Name the blood parasite species.
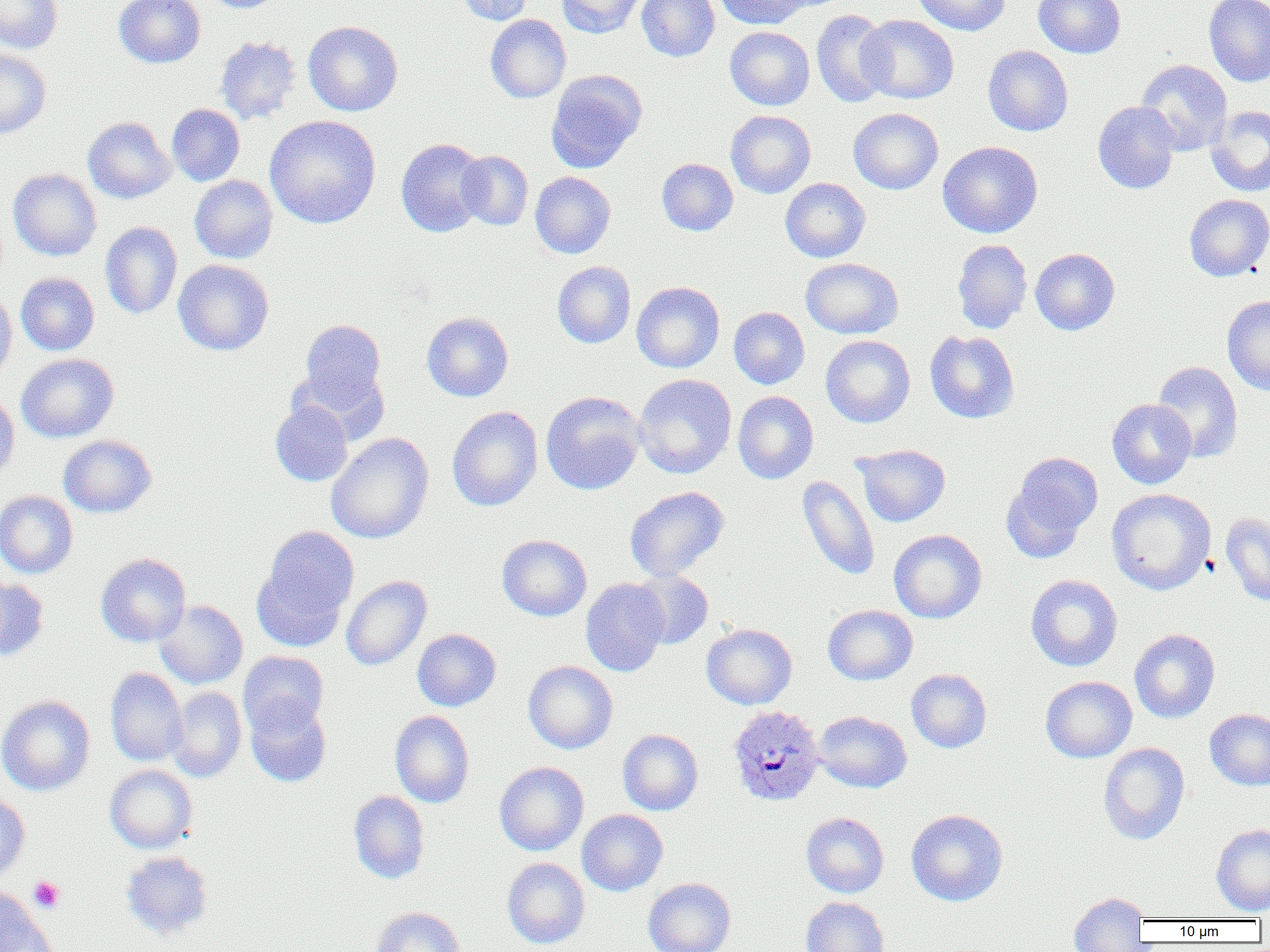
Plasmodium ovale.

{
  "platelet_locations": "approximate bounding boxes as [x1, y1, x2, y2] in pixels: [29, 876, 64, 912]",
  "preparation": "thin blood smear",
  "uninfected_red_blood_cell_locations": "approximate bounding boxes as [x1, y1, x2, y2] in pixels: [0, 0, 62, 53], [114, 0, 205, 68], [206, 0, 285, 13], [452, 0, 535, 25], [556, 0, 646, 38], [636, 0, 720, 62], [714, 0, 811, 29], [912, 0, 1010, 35], [1034, 0, 1126, 59], [1204, 0, 1270, 87], [811, 9, 892, 108], [485, 14, 571, 103], [856, 15, 959, 104], [303, 21, 403, 116], [725, 26, 815, 110], [215, 36, 301, 125], [983, 45, 1073, 136], [0, 48, 51, 139], [1135, 59, 1233, 155], [546, 70, 647, 173], [1092, 101, 1181, 194], [166, 104, 244, 186], [1206, 105, 1270, 197], [848, 107, 943, 194], [726, 110, 816, 198], [264, 114, 381, 228], [82, 116, 175, 204], [396, 138, 488, 238], [937, 141, 1042, 238], [456, 151, 533, 230], [657, 158, 738, 235], [8, 169, 102, 261], [530, 172, 615, 258], [189, 175, 277, 263], [780, 178, 870, 263], [1184, 194, 1270, 281], [100, 222, 182, 319], [952, 239, 1032, 333], [1030, 248, 1120, 335], [801, 258, 903, 339], [173, 259, 274, 356], [552, 261, 636, 348], [15, 272, 99, 356], [632, 282, 724, 372], [0, 289, 17, 388], [1222, 295, 1270, 395], [729, 307, 809, 389], [422, 312, 513, 402], [299, 319, 386, 408], [925, 330, 1019, 423], [821, 335, 915, 428], [16, 353, 118, 442], [1152, 361, 1243, 462], [634, 374, 736, 479], [0, 391, 19, 481], [541, 391, 645, 495], [733, 391, 818, 484], [1107, 399, 1196, 489], [270, 401, 352, 486], [447, 406, 543, 512], [326, 433, 433, 543], [58, 435, 156, 518], [853, 444, 950, 527], [1002, 452, 1102, 559], [797, 475, 880, 580], [625, 486, 729, 581], [1106, 488, 1216, 594], [0, 490, 78, 578], [1220, 512, 1270, 606], [254, 526, 359, 647], [888, 529, 987, 623], [496, 534, 592, 621], [96, 553, 191, 646], [630, 570, 713, 649], [1025, 574, 1123, 672], [340, 575, 432, 670], [0, 577, 48, 661], [581, 578, 669, 676], [154, 599, 248, 689], [823, 605, 917, 685], [701, 623, 797, 710], [412, 629, 501, 711], [1129, 629, 1220, 723], [238, 651, 329, 735], [523, 661, 618, 754], [105, 668, 188, 766], [906, 668, 992, 753], [1040, 676, 1137, 763], [167, 687, 246, 782], [0, 695, 95, 796], [244, 695, 331, 787], [1205, 709, 1270, 791], [390, 711, 474, 807], [813, 711, 912, 793], [618, 729, 703, 815], [1098, 742, 1190, 845], [494, 762, 589, 855], [105, 765, 197, 853], [348, 790, 430, 883], [0, 794, 30, 884], [577, 809, 668, 896], [906, 809, 1008, 906], [801, 812, 889, 898], [1210, 824, 1270, 915], [120, 850, 213, 939], [502, 858, 590, 948], [643, 877, 736, 952], [0, 886, 39, 951], [1068, 892, 1149, 951], [801, 897, 889, 952], [371, 906, 466, 952], [2, 909, 59, 952]",
  "image_size": "1270×952 pixels",
  "plasmodium_ovale_infected_red_blood_cell_locations": "approximate bounding boxes as [x1, y1, x2, y2] in pixels: [728, 704, 825, 807]",
  "modality": "optical microscopy",
  "magnification": "1000x",
  "field_of_view": "one of a larger specimen"
}